Identify the cell.
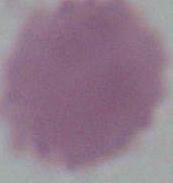
This is an erythrocyte.

Micrograph. Captured at 1000x magnification.